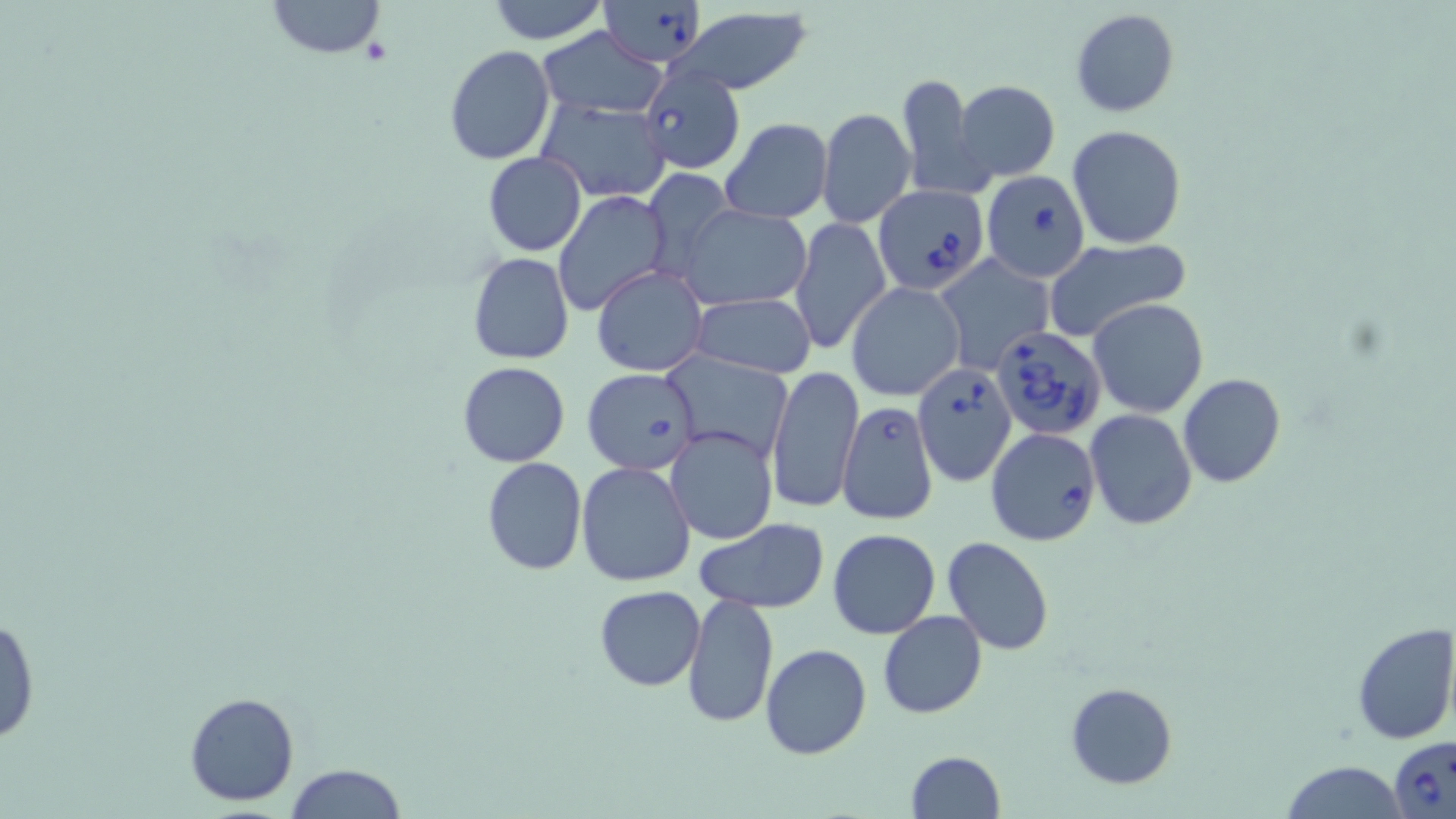
{
  "slide_level_diagnosis": "Babesia divergens",
  "uninfected_red_blood_cell_locations": "approximate bounding boxes as [x1, y1, x2, y2] in pixels: [265, 0, 387, 58], [484, 0, 610, 44], [667, 7, 816, 96], [1070, 8, 1179, 116], [538, 26, 666, 119], [443, 45, 556, 165], [897, 71, 992, 203], [955, 80, 1060, 182], [537, 98, 671, 203], [816, 107, 916, 229], [720, 119, 833, 222], [704, 122, 824, 308], [1066, 124, 1188, 250], [484, 153, 586, 256], [643, 168, 732, 275], [554, 191, 670, 315], [679, 203, 812, 311], [791, 217, 892, 355], [1043, 238, 1191, 344], [467, 252, 573, 365], [935, 255, 1053, 372], [592, 265, 708, 378], [846, 282, 966, 402], [688, 293, 817, 379], [1089, 298, 1208, 418], [667, 354, 792, 462], [458, 361, 568, 467], [767, 365, 864, 514], [581, 367, 703, 476], [1178, 374, 1287, 488], [1086, 409, 1197, 529], [665, 426, 778, 545], [480, 456, 587, 576], [575, 461, 698, 587], [693, 517, 832, 614], [828, 528, 939, 638], [942, 537, 1055, 654], [593, 585, 707, 691], [683, 592, 778, 728], [0, 610, 40, 747], [878, 610, 987, 719], [1350, 622, 1456, 745], [759, 643, 872, 759], [1065, 682, 1177, 789], [183, 691, 300, 806], [904, 749, 1007, 818], [1282, 761, 1410, 818], [279, 764, 408, 819]",
  "image_size": "1456×819 pixels",
  "modality": "optical microscopy",
  "magnification": "1000x",
  "preparation": "thin blood film",
  "field_of_view": "single",
  "babesia_divergens_infected_red_blood_cell_locations": "approximate bounding boxes as [x1, y1, x2, y2] in pixels: [601, 1, 706, 66], [637, 62, 747, 174], [981, 170, 1091, 281], [873, 185, 988, 294], [991, 329, 1108, 442], [912, 361, 1017, 487], [836, 398, 938, 527], [987, 428, 1100, 543], [1389, 737, 1456, 819]",
  "stain": "May-Grünwald-Giemsa"
}